Give the position of every Plasmodium parasite.
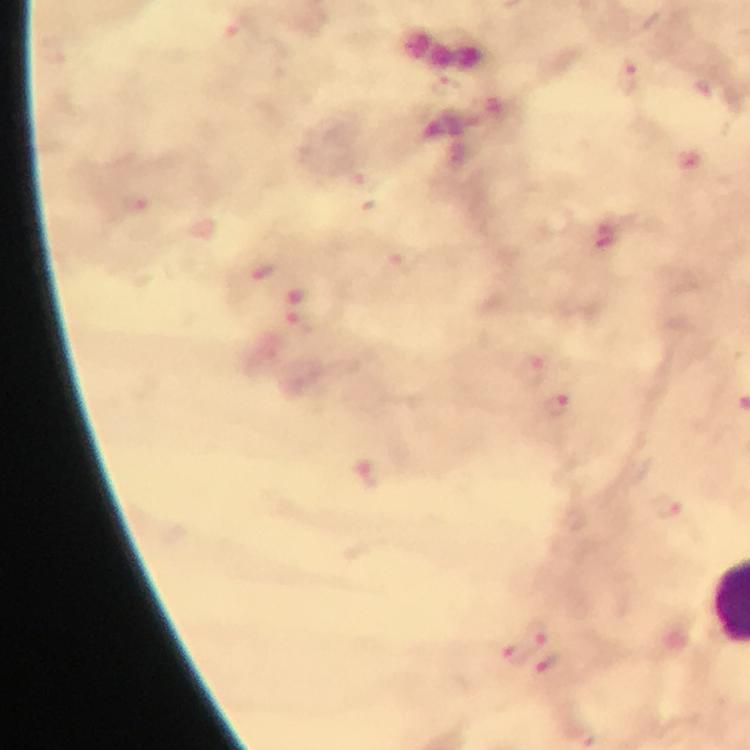

Approximate centers as (x, y) in pixels.
Plasmodium parasites: (237, 27), (631, 80), (265, 271), (530, 368), (560, 405), (368, 474), (668, 509), (535, 635), (511, 658), (550, 662).

From a malaria diagnostic workup. A crop from one field of view. Giemsa stain. Immersion oil was used. Smartphone photograph taken through a microscope. Thick blood film. At 100x magnification. Image is 750×750 pixels.